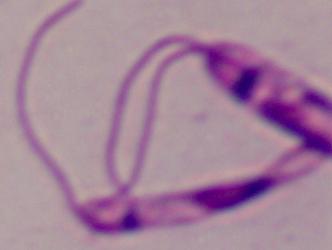

Summary:
  - Magnification: 1000x
  - Identification: Leishmania
  - Modality: photomicrograph